Describe the morphology of the red blood cells.
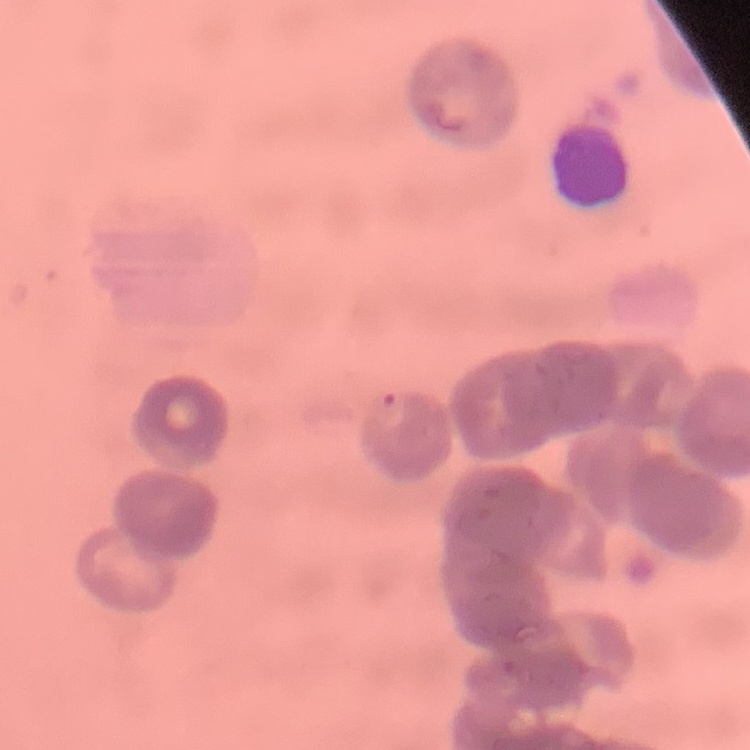
Rouleaux formation.

Stained with either Field's or Giemsa. Thin blood smear. One tile cut from a larger photomicrograph.